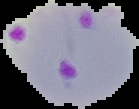
Malaria status: parasitized. Segmented cell region on a black background. Image is 139×109 pixels. From a thin blood smear.